Report the malaria status of this cell.
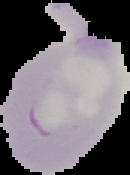
Parasitized.

Cell region segmented out of the field of view; the surrounding area is masked to black. Image is 130×175 pixels. From a thin blood smear.